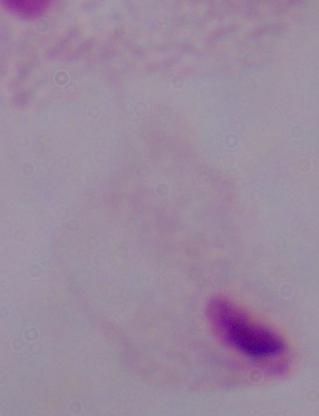
A trichomonad is shown. 1000x magnification. Photomicrograph.